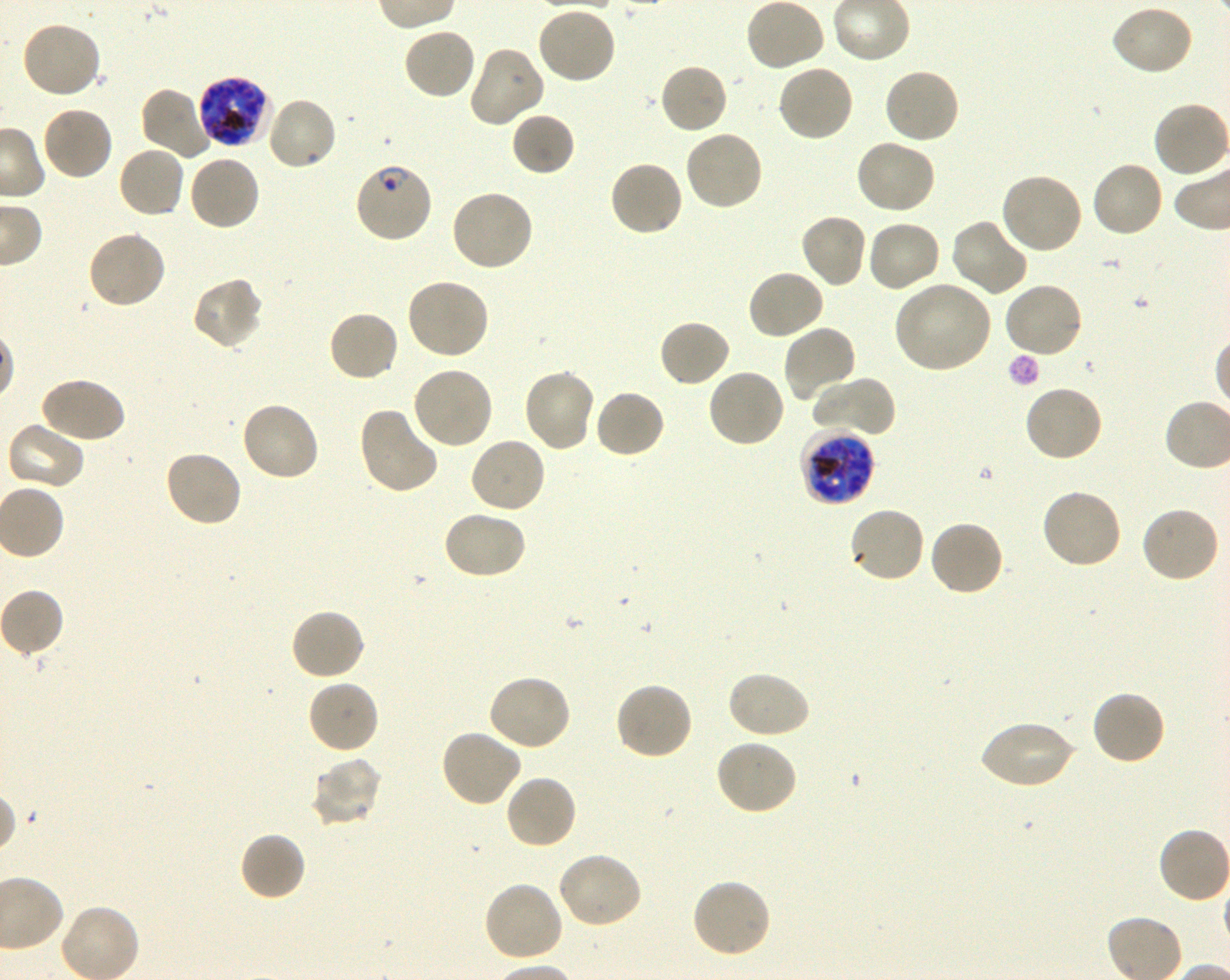

Not every red blood cell is marked. A life-cycle stage — or a range of stages, where the recorded stages span more than one — follows each staged infected red blood cell.
field of view = single
objective = 100x, oil immersion, numerical aperture 1.30
donor blood group = O+
preparation = thin blood smear
locations of infected red blood cells = approximate bounding boxes as (x1, y1, x2, y2) in pixels: (196, 75, 271, 149) late trophozoite to late schizont; (354, 161, 434, 244) ring; (800, 427, 876, 506) late trophozoite to late schizont
image size = 1230×980 pixels
locations of uninfected red blood cells = approximate bounding boxes as (x1, y1, x2, y2) in pixels: (744, 0, 826, 72), (535, 4, 617, 84), (1108, 4, 1194, 78), (20, 21, 104, 100), (403, 27, 477, 101), (467, 44, 545, 128), (658, 62, 728, 135), (776, 62, 856, 142), (882, 67, 961, 144), (139, 86, 214, 161), (265, 95, 338, 171), (1152, 101, 1230, 180), (40, 105, 114, 181), (510, 111, 576, 177), (683, 129, 765, 212), (853, 138, 937, 216), (117, 145, 186, 219), (187, 153, 261, 232), (607, 160, 684, 237), (1090, 161, 1165, 239), (999, 171, 1085, 256), (449, 187, 535, 272), (799, 212, 868, 289), (950, 218, 1028, 297), (865, 219, 943, 294), (86, 229, 167, 310), (746, 269, 826, 341), (191, 277, 264, 351), (405, 277, 490, 360), (1003, 280, 1085, 358), (891, 286, 997, 368), (327, 310, 400, 384), (657, 318, 731, 388), (782, 325, 859, 404), (409, 365, 494, 449), (706, 367, 787, 449), (522, 368, 597, 453), (38, 376, 126, 445), (809, 376, 897, 436), (1022, 385, 1103, 464), (593, 389, 667, 460), (239, 400, 320, 482), (358, 405, 440, 496), (4, 420, 85, 491), (468, 435, 547, 514), (163, 449, 243, 528), (1040, 488, 1124, 570), (847, 505, 926, 584), (1140, 505, 1221, 584), (441, 509, 527, 581), (927, 519, 1004, 597), (290, 607, 367, 681), (725, 670, 810, 740), (486, 673, 573, 751), (306, 680, 379, 756), (614, 680, 694, 761), (1090, 690, 1167, 767), (977, 719, 1075, 790), (440, 729, 523, 808), (714, 739, 798, 817), (310, 758, 382, 828), (503, 773, 579, 851), (1157, 826, 1230, 904), (238, 831, 306, 902), (556, 851, 643, 929), (691, 877, 771, 960), (482, 881, 565, 963)
stain = Giemsa
culture = in-vitro P. falciparum strain 3D7, shaking